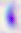

identification = Toxoplasma gondii
magnification = 400x
modality = photomicrograph